Point out each malaria parasite.
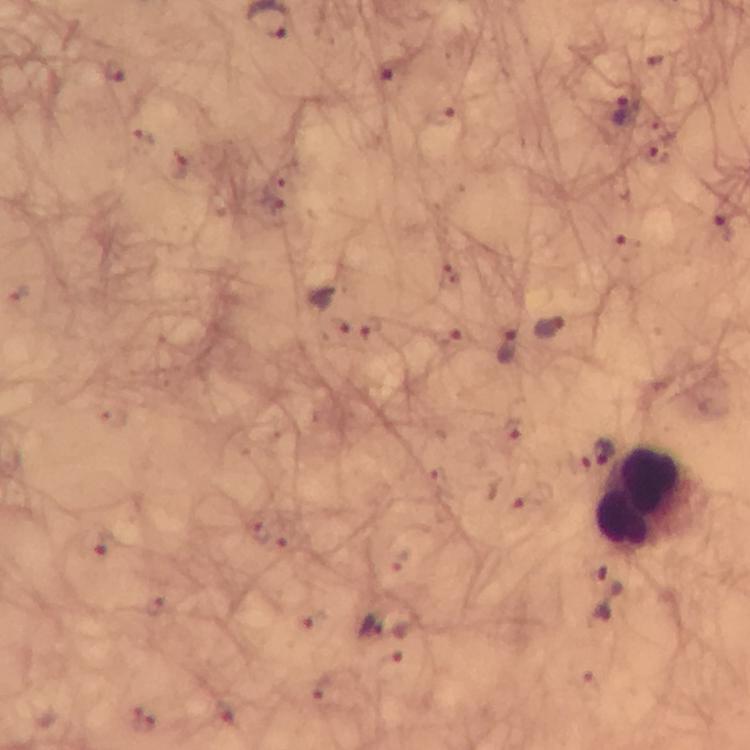
Approximate centers as [x, y] in pixels.
Malaria parasites: [388, 76], [620, 113], [725, 227], [629, 249], [548, 328], [456, 341], [507, 346], [534, 499], [606, 595], [370, 627].

Summary:
  - Leukocyte locations: [650, 498]
  - Magnification: 100x
  - Context: from a diagnostic examination for malaria
  - Image size: 750×750 pixels
  - Cropped from: one field of view
  - Immersion oil: applied
  - Capture: smartphone photograph through a microscope
  - Stain: Giemsa
  - Preparation: thick blood film